Name the cell type shown.
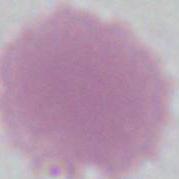
An erythrocyte.

Summary:
  - Magnification: 1000x
  - Modality: micrograph